Locate every uninfected red blood cell.
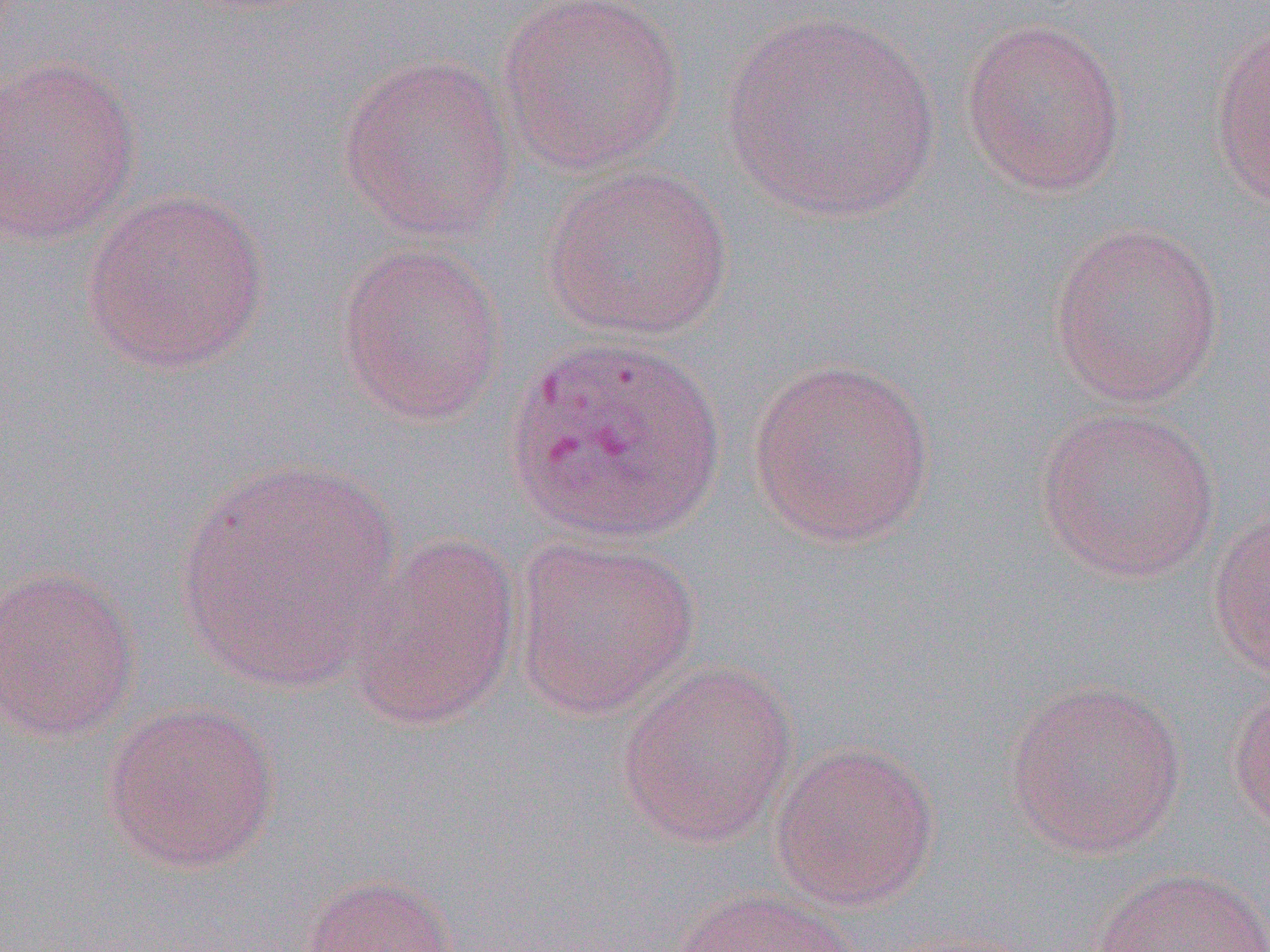

Approximate bounding boxes as (x1,y1)-(x2,y2) corner pairs in pixels.
Uninfected red blood cells: (495,0)-(686,176), (722,10)-(942,224), (960,16)-(1129,198), (1206,17)-(1270,213), (337,52)-(518,243), (0,54)-(142,247), (541,163)-(735,342), (80,188)-(272,375), (1047,220)-(1225,407), (334,240)-(507,427), (746,355)-(938,547), (1034,404)-(1221,583), (175,458)-(404,694), (1207,502)-(1270,683), (343,530)-(522,731), (509,532)-(702,721), (0,564)-(140,745), (615,660)-(799,848), (1002,678)-(1188,858), (1227,678)-(1270,836), (101,700)-(281,874), (769,740)-(940,912), (1092,865)-(1270,952), (295,872)-(461,952), (670,886)-(864,952).

Slide-level diagnosis: Plasmodium vivax. Thin blood film. Light microscopy. Image is 1270×952 pixels. Captured at 1000x magnification. One field of a larger specimen.